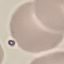

malaria_status: uninfected
preparation: thin blood film
image_type: automatically extracted cell patch, resized to 64 × 64 pixels
capture: smartphone camera at the microscope eyepiece
stain: Giemsa